Classify this cell by malaria status.
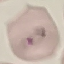
It is parasitized.

Summary:
  - Capture: smartphone camera at the microscope eyepiece
  - Stain: Giemsa
  - Image type: cell patch, automatically extracted from a larger field of view and resized to 64 × 64 pixels
  - Preparation: thin smear